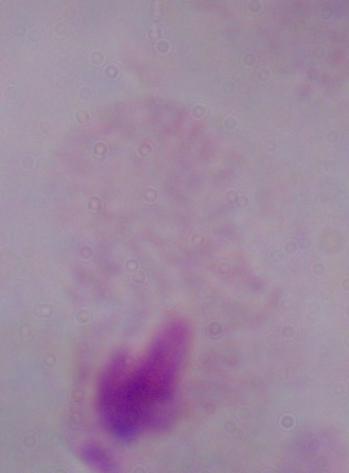 A trichomonad is shown. Photomicrograph. 1000x magnification.